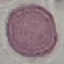
Summary:
  - Malaria status: uninfected
  - Capture: smartphone through the microscope eyepiece
  - Preparation: thin smear
  - Image type: cell patch, automatically extracted from a larger field of view and resized to 64 × 64 pixels
  - Stain: Giemsa